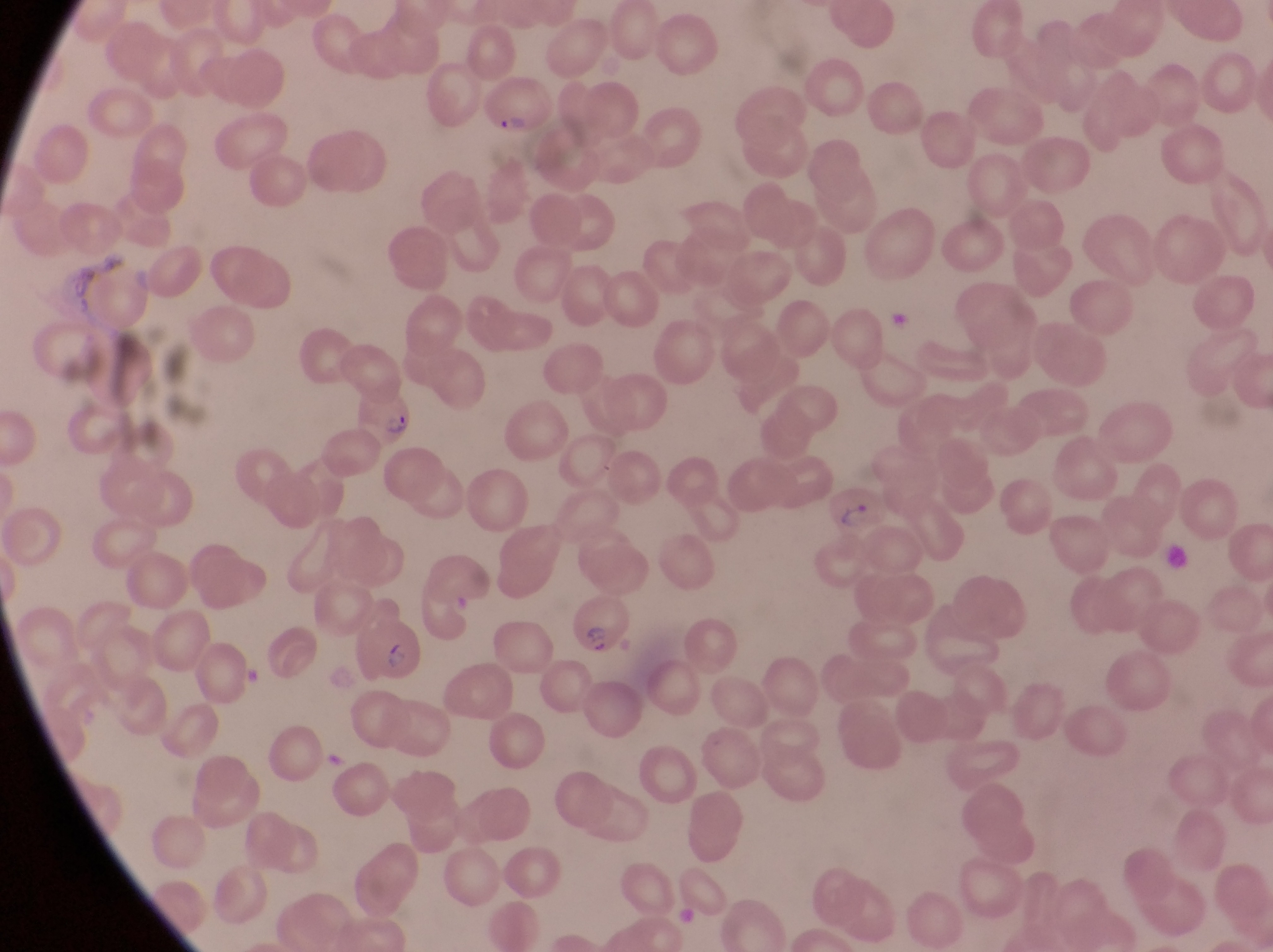
capture: smartphone photograph through the eyepiece of an Olympus CX-23 microscope
field_of_view: single
magnification: 1000x
preparation: thin blood smear
parasitised_red_blood_cell_locations: 'approximate bounding boxes as left top right bottom in pixels: 485 80 552 133; 350 377 422 452; 826 487 891 539; 567 596 630 661; 356 614 426 684'
image_size: 1273×952 pixels
country: Uganda
artifact_platelet_like_body_stain_precipitate_or_debris_locations: 'approximate bounding boxes as left top right bottom in pixels: 1162 544 1194 582'